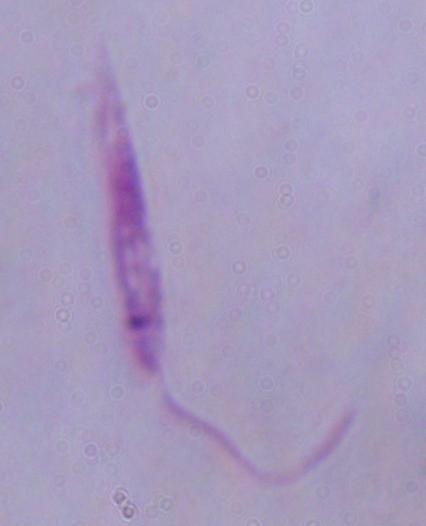
modality = photomicrograph
magnification = 1000x
identification = Leishmania